Outline each uninfected red blood cell.
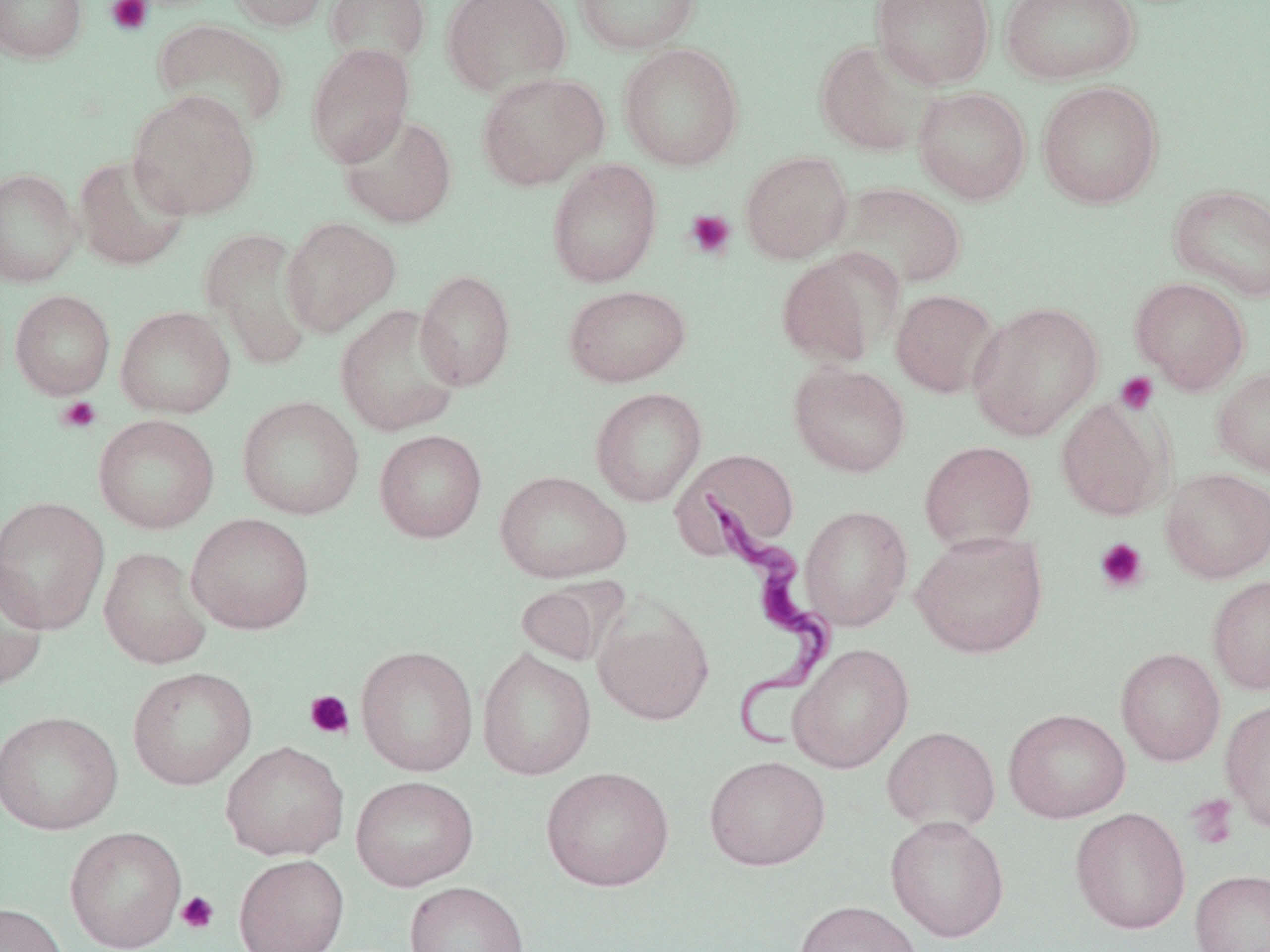
Approximate bounding boxes as (x1,y1)-(x2,y2) corner pairs in pixels.
Uninfected red blood cells: (0,0)-(87,63), (226,0)-(333,32), (325,0)-(430,69), (441,0)-(572,97), (573,0)-(702,55), (871,0)-(995,89), (1000,0)-(1141,85), (153,19)-(289,132), (813,39)-(938,157), (618,42)-(744,171), (305,43)-(415,167), (476,72)-(609,190), (1036,81)-(1164,208), (913,86)-(1031,205), (127,89)-(260,220), (338,113)-(457,228), (740,151)-(853,264), (73,153)-(191,271), (547,158)-(663,288), (0,168)-(82,287), (832,182)-(967,291), (1167,184)-(1270,301), (281,217)-(401,337), (201,227)-(317,370), (775,249)-(899,368), (415,269)-(516,391), (1129,277)-(1251,394), (564,284)-(691,387), (891,289)-(999,398), (10,290)-(115,399), (968,301)-(1104,441), (335,304)-(464,437), (115,305)-(236,418), (788,362)-(911,477), (1212,367)-(1270,478), (590,387)-(707,506), (236,395)-(364,520), (1055,396)-(1170,521), (93,414)-(220,534), (374,429)-(487,543), (919,441)-(1037,553), (674,449)-(800,554), (1160,467)-(1270,583), (494,470)-(631,583), (0,495)-(110,636), (799,505)-(913,631), (185,512)-(315,634), (911,530)-(1048,658), (99,546)-(212,669), (0,558)-(49,693), (1207,576)-(1270,694), (515,579)-(621,667), (594,601)-(714,726), (788,643)-(914,774), (356,645)-(478,776), (477,647)-(597,780), (1116,648)-(1225,766), (127,666)-(257,790), (1220,698)-(1270,834), (1003,708)-(1131,823), (0,709)-(123,836), (882,726)-(1001,834), (220,741)-(349,861), (704,755)-(830,871), (540,765)-(675,891), (351,775)-(478,891), (1070,807)-(1191,934), (885,815)-(1010,942), (64,826)-(187,952), (233,854)-(349,952), (1189,869)-(1270,952), (403,881)-(529,952), (793,900)-(922,952), (0,901)-(70,952).

Platelet locations: (105,0)-(154,36), (684,209)-(736,260), (1115,372)-(1158,416), (56,396)-(102,434), (1094,537)-(1149,594), (304,689)-(354,740), (1186,793)-(1240,850), (176,891)-(219,934). Trypanosoma brucei locations: (690,489)-(839,753). Slide-level diagnosis: Trypanosoma brucei. 1000x magnification. May-Grünwald-Giemsa stain. One field of a larger specimen. Thin blood film. Light microscopy. Image is 1270×952 pixels.